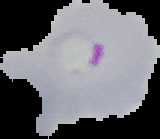
image size = 160×139 pixels
malaria status = parasitized
preparation = thin blood smear
image type = cell region segmented out of the field of view; surrounding area masked to black